Give the position of every leukocyte visible.
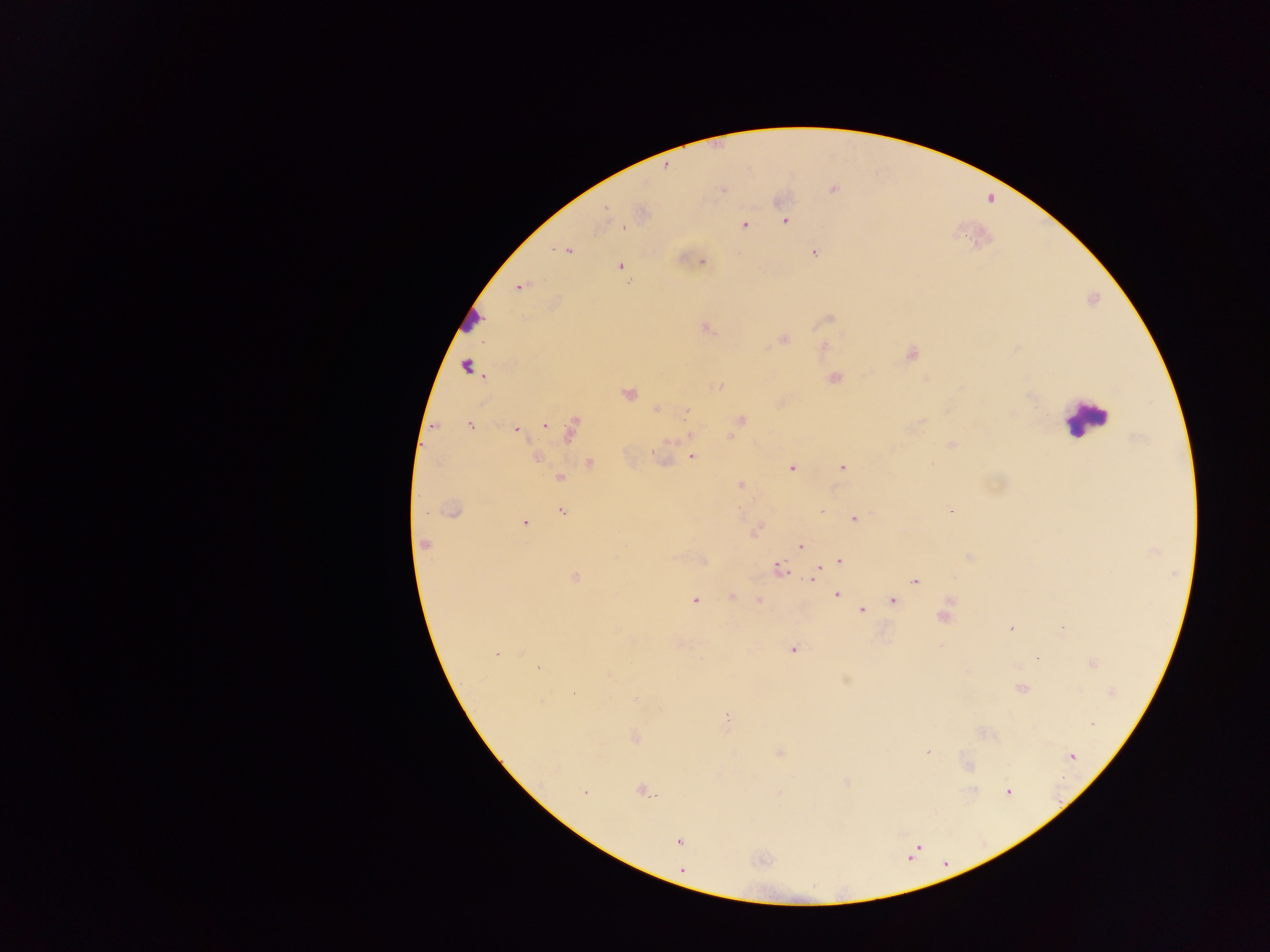
Approximate centers as [x, y] in pixels.
Leukocytes: [467, 321], [1085, 418].

{
  "image_size": "1270×952 pixels",
  "country": "Ghana",
  "plasmodium_parasite_locations": "approximate centers as [x, y] in pixels: [666, 167], [722, 190], [606, 207], [785, 221], [745, 224], [623, 227], [568, 251], [814, 253], [701, 261], [620, 266], [521, 286], [829, 318], [707, 328], [783, 339], [824, 345], [912, 354], [466, 365], [835, 378], [719, 386], [629, 393], [657, 409], [687, 411], [741, 420], [544, 425], [470, 426], [516, 429], [570, 429], [690, 436], [950, 445], [692, 456], [536, 458], [590, 463], [842, 467], [792, 468], [560, 479], [741, 485], [951, 510], [453, 511], [561, 511], [425, 512], [854, 518], [524, 523], [424, 544], [800, 547], [970, 557], [839, 561], [779, 568], [574, 578], [814, 578], [915, 580], [837, 595], [732, 596], [695, 600], [759, 600], [893, 600], [862, 610], [944, 617], [1062, 627], [1010, 628], [793, 650], [497, 653], [538, 667], [1022, 689], [574, 692], [636, 700], [727, 716], [1093, 723], [635, 738], [927, 752], [780, 753], [1072, 756], [846, 782], [642, 791], [1008, 792], [585, 793], [679, 842], [682, 869]",
  "preparation": "thick blood film",
  "capture": "mobile-phone photograph through a microscope",
  "field_of_view": "single"
}